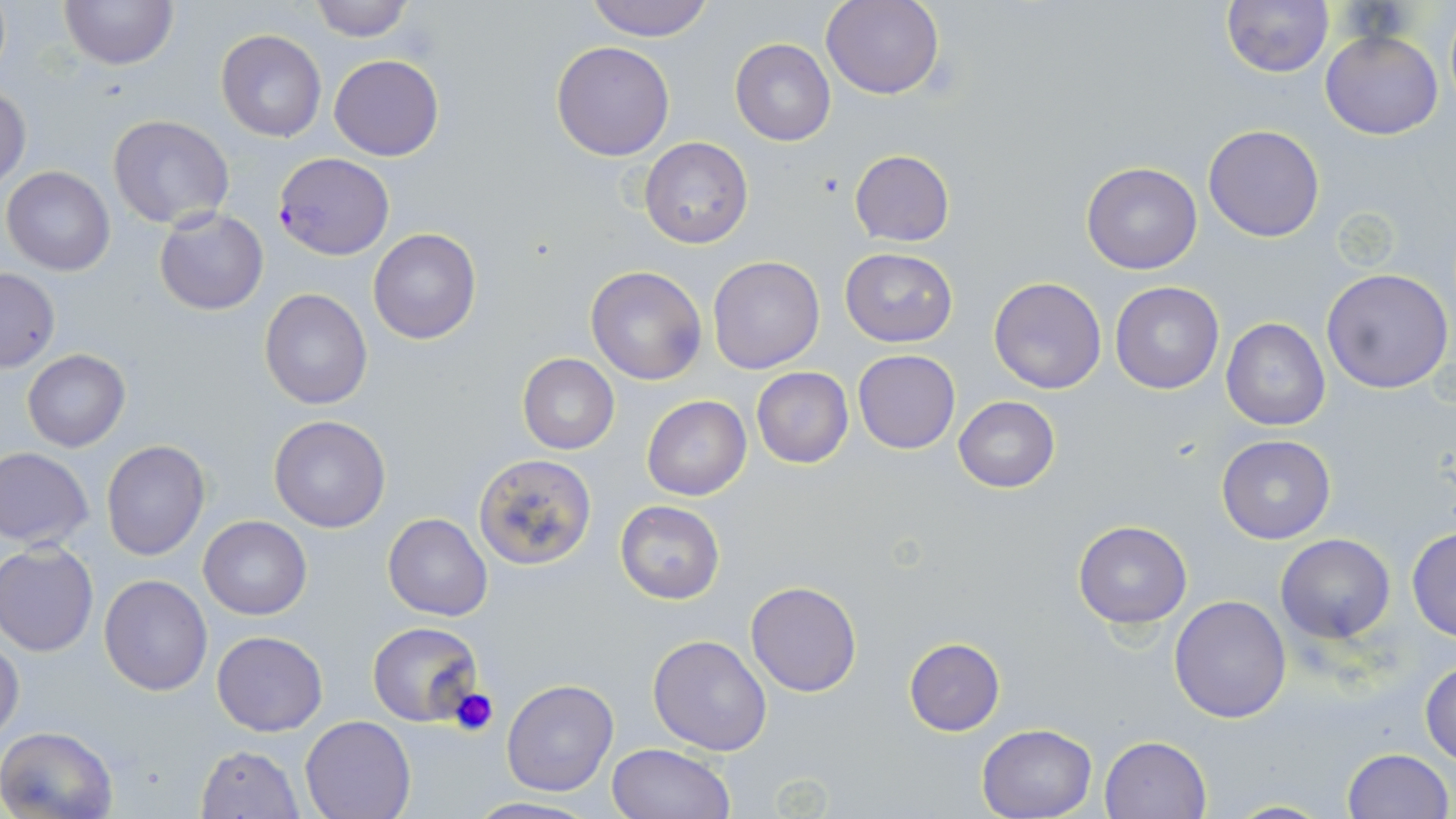

Approximate bounding boxes as (x1,y1)-(x2,y2) corner pairs in pixels. Uninfected red blood cell locations: (59,0)-(180,69), (584,0)-(717,41), (1221,0)-(1335,77), (308,1)-(416,41), (820,1)-(945,100), (216,29)-(327,142), (1320,30)-(1444,140), (731,38)-(836,147), (551,40)-(675,160), (329,54)-(444,161), (0,85)-(30,187), (108,114)-(234,228), (1203,123)-(1325,242), (640,137)-(753,250), (848,149)-(955,247), (1081,162)-(1202,275), (2,166)-(116,275), (154,208)-(269,314), (368,228)-(481,345), (839,248)-(957,346), (708,255)-(825,374), (584,265)-(706,385), (1321,267)-(1454,395), (1,269)-(59,372), (988,276)-(1107,394), (1110,280)-(1224,394), (259,288)-(372,410), (1220,318)-(1331,430), (23,350)-(129,452), (852,350)-(961,454), (517,353)-(620,455), (750,366)-(854,469), (641,394)-(751,502), (952,396)-(1061,493), (268,416)-(391,532), (1216,434)-(1336,545), (101,440)-(210,559), (0,447)-(94,549), (473,453)-(597,568), (615,501)-(725,603), (384,514)-(492,621), (199,515)-(311,619), (1072,521)-(1192,630), (1408,527)-(1456,642), (1276,534)-(1395,642), (1,542)-(99,656), (100,574)-(211,695), (746,580)-(862,697), (1169,594)-(1292,723), (366,621)-(484,726), (213,630)-(328,736), (648,634)-(774,755), (0,636)-(24,744), (903,636)-(1005,735), (1420,659)-(1456,765), (501,678)-(619,795), (301,715)-(415,818), (977,723)-(1095,818), (0,726)-(118,819), (1100,736)-(1211,819), (607,743)-(732,819), (196,745)-(304,818), (1341,747)-(1454,818), (465,795)-(601,818). Platelet locations: (447,685)-(501,736). Plasmodium falciparum-infected red blood cell locations: (274,151)-(394,261). Slide-level diagnosis: Plasmodium falciparum. Thin blood smear. Image is 1456×819 pixels. Captured at 1000x magnification. May-Grünwald-Giemsa-stained preparation. Light microscopy. One field of a larger specimen.